Name the parasite shown.
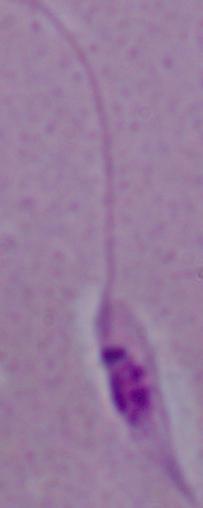
Leishmania.

Micrograph. 1000x magnification.